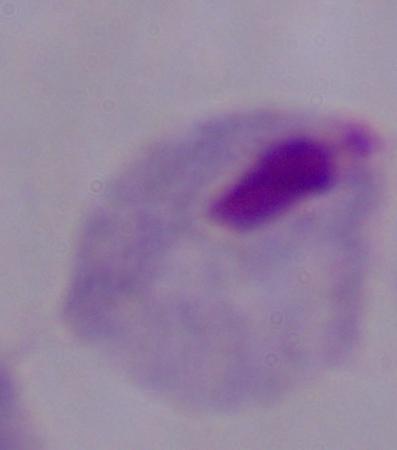 Captured at 1000x magnification. Photomicrograph. A trichomonad is shown.